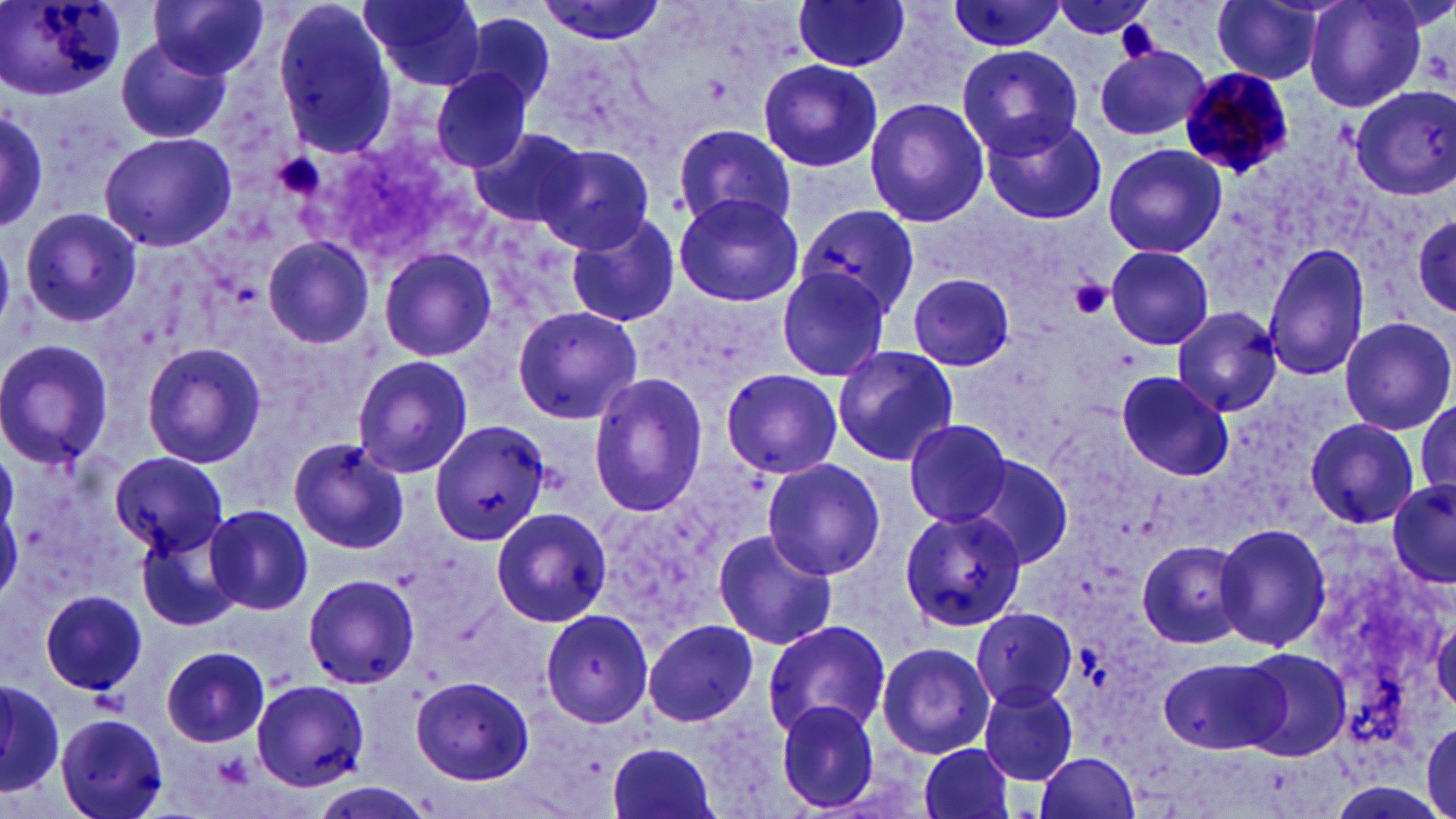

slide-level diagnosis = Plasmodium malariae
modality = optical microscopy
image size = 1456×819 pixels
platelet locations = approximate bounding boxes as [x1, y1, x2, y2] in pixels: [1069, 277, 1113, 320], [214, 750, 254, 791]
stain = May-Grünwald-Giemsa
Plasmodium malariae-infected red blood cell locations = approximate bounding boxes as [x1, y1, x2, y2] in pixels: [1177, 66, 1298, 177]
uninfected red blood cell locations = approximate bounding boxes as [x1, y1, x2, y2] in pixels: [2, 0, 124, 100], [151, 0, 267, 79], [533, 0, 668, 47], [791, 0, 913, 73], [941, 0, 1069, 52], [1050, 0, 1160, 44], [1211, 0, 1329, 84], [1304, 0, 1429, 113], [360, 1, 484, 89], [270, 3, 398, 157], [460, 11, 557, 117], [117, 38, 231, 145], [958, 44, 1083, 157], [1095, 45, 1210, 142], [759, 59, 882, 172], [431, 67, 534, 173], [1347, 84, 1456, 201], [864, 97, 990, 228], [0, 104, 48, 230], [983, 111, 1110, 223], [671, 122, 796, 234], [469, 126, 589, 231], [100, 132, 235, 251], [1101, 142, 1228, 260], [536, 144, 656, 254], [670, 193, 803, 307], [797, 205, 919, 320], [20, 207, 141, 327], [565, 212, 683, 329], [1412, 212, 1455, 318], [262, 235, 373, 349], [1264, 241, 1372, 381], [378, 245, 498, 363], [1103, 245, 1214, 351], [774, 267, 892, 382], [907, 273, 1016, 372], [510, 304, 643, 424], [1171, 305, 1282, 416], [1339, 316, 1454, 434], [0, 339, 115, 469], [141, 343, 267, 468], [831, 344, 957, 465], [352, 356, 474, 477], [721, 369, 843, 480], [1115, 369, 1235, 481], [587, 373, 709, 516], [1414, 398, 1455, 502], [902, 417, 1014, 526], [1304, 418, 1422, 528], [432, 420, 547, 547], [289, 438, 409, 555], [111, 450, 225, 558], [968, 452, 1075, 571], [763, 459, 884, 579], [1386, 480, 1456, 591], [1, 494, 23, 605], [206, 504, 315, 615], [491, 504, 613, 627], [899, 505, 1026, 633], [1212, 523, 1330, 650], [139, 529, 240, 633], [710, 530, 839, 650], [1137, 538, 1250, 649], [302, 572, 421, 689], [41, 588, 148, 697], [971, 607, 1078, 709], [541, 610, 655, 728], [1431, 613, 1455, 716], [643, 618, 760, 729], [762, 619, 891, 740], [876, 641, 994, 758], [162, 645, 271, 746], [1234, 646, 1352, 761], [1157, 655, 1283, 755], [412, 676, 532, 783], [252, 679, 373, 790], [1, 681, 64, 795], [978, 683, 1081, 787], [772, 700, 883, 814], [56, 713, 170, 819], [1424, 718, 1456, 814], [605, 739, 719, 819], [916, 742, 1016, 819], [1033, 751, 1140, 819], [314, 783, 434, 818]
field of view = single
preparation = thin blood film
magnification = 1000x